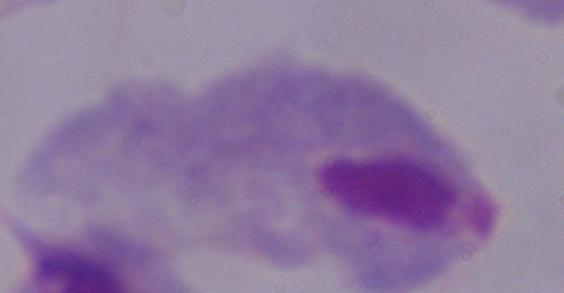

identification = trichomonad
modality = photomicrograph
magnification = 1000x